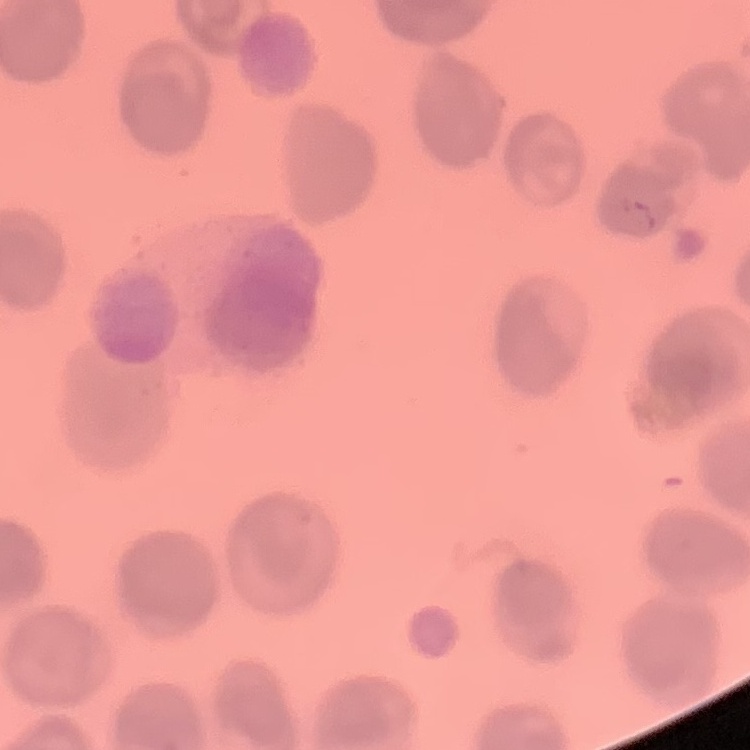
Summary:
  - Erythrocyte morphology: no rouleaux formation
  - Preparation: thin peripheral smear
  - Stain: Field's or Giemsa
  - Image type: square crop of a larger photomicrograph